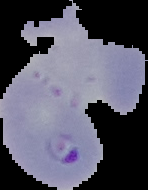
{
  "result": "malaria parasites detected",
  "preparation": "thin blood film",
  "image_type": "segmented cell region on a black background",
  "image_size": "148×190 pixels"
}